Name the parasite shown.
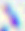
This is Toxoplasma gondii.

Summary:
  - Magnification: 400x
  - Modality: micrograph